Assess this cell for malaria.
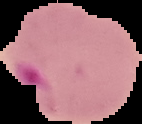
It is parasitized.

Summary:
  - Image type: segmented cell region on a black background
  - Image size: 142×124 pixels
  - Preparation: thin blood smear